Identify the parasite.
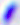

Toxoplasma gondii.

Summary:
  - Modality: photomicrograph
  - Magnification: 400x